Assess this cell for malaria.
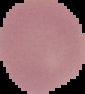
Uninfected.

{
  "image_type": "segmented cell region on a black background",
  "preparation": "thin blood film",
  "image_size": "85×94 pixels"
}